Assess this cell for malaria.
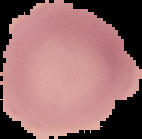
It is uninfected.

Image is 142×139 pixels. From a thin blood film. Cell region segmented out of the field of view; the surrounding area is masked to black.